Classify this cell by malaria status.
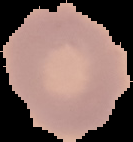

It is uninfected.

Summary:
  - Image size: 133×142 pixels
  - Image type: cell region segmented out of the field of view; surrounding area masked to black
  - Preparation: thin blood film